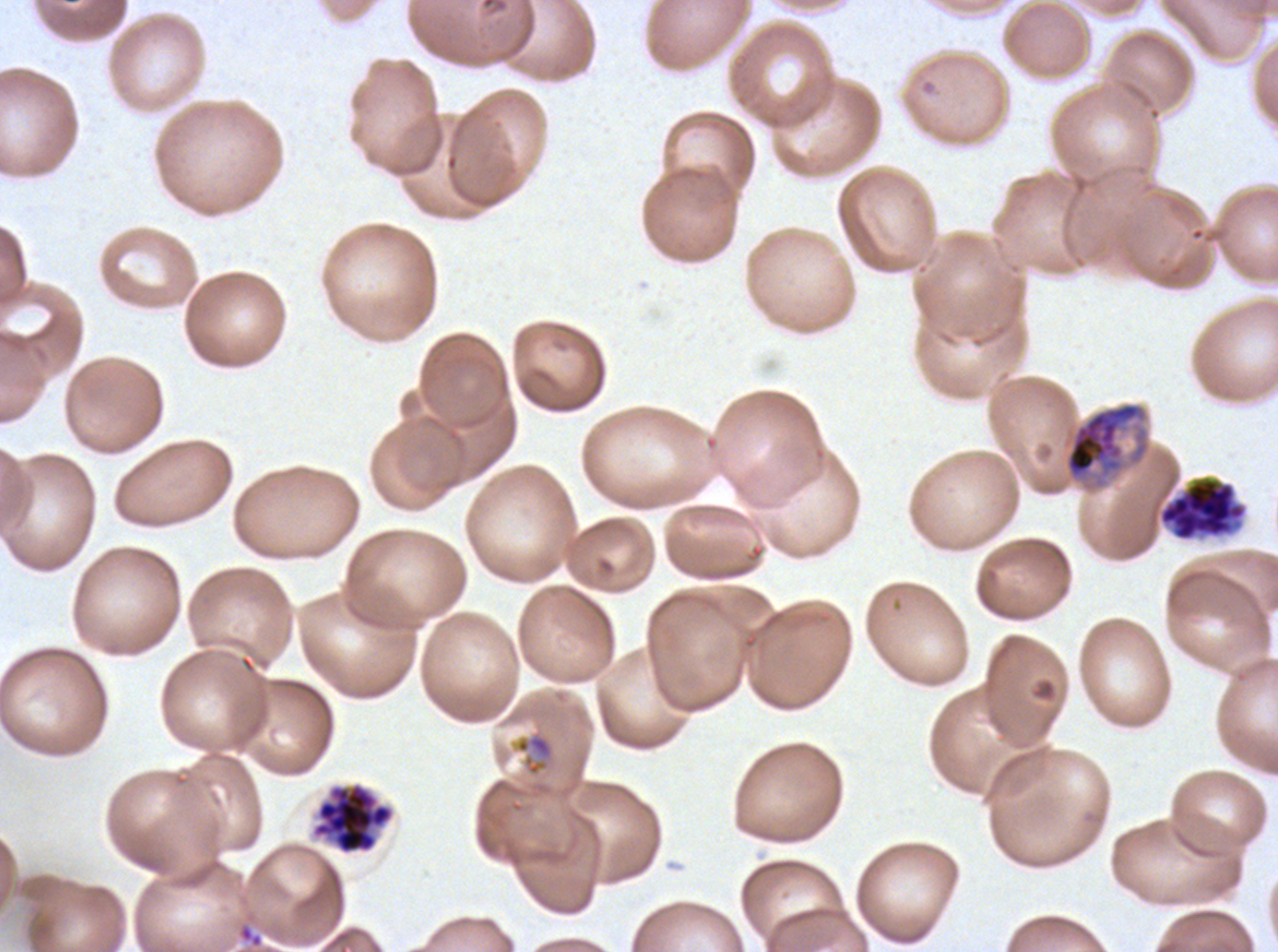
notation = approximate bounding boxes as {x1, y1, x2, y2} in pixels
segmenter locations = {1157, 475, 1248, 542}, {312, 782, 394, 855}
early schizont locations = {1063, 401, 1151, 493}
late-ring/early-trophozoite locations = {515, 733, 554, 776}
specimen = ex-vivo Plasmodium falciparum culture from a patient in The Gambia, grown for 24 to 48 hours
life-cycle stages observed = late-ring/early-trophozoite, early schizont, segmenter
preparation = thin blood smear
image size = 1278×952 pixels
stain = Giemsa
field of view = one sub-image of a larger composite